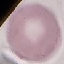

Malaria status: uninfected. Thin blood film. Automatically extracted cell patch, resized to 64 × 64 pixels. Giemsa stain. Acquired by smartphone through the microscope eyepiece.